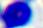 A leukocyte is seen. Micrograph. Captured at 400x magnification.